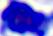

Summary:
  - Modality: micrograph
  - Magnification: 400x
  - Identification: white blood cell